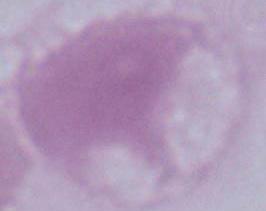

identification: erythrocyte
magnification: 1000x
modality: photomicrograph